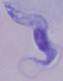
identification = trypanosome
modality = micrograph
magnification = 1000x